Evaluate for Plasmodium parasites.
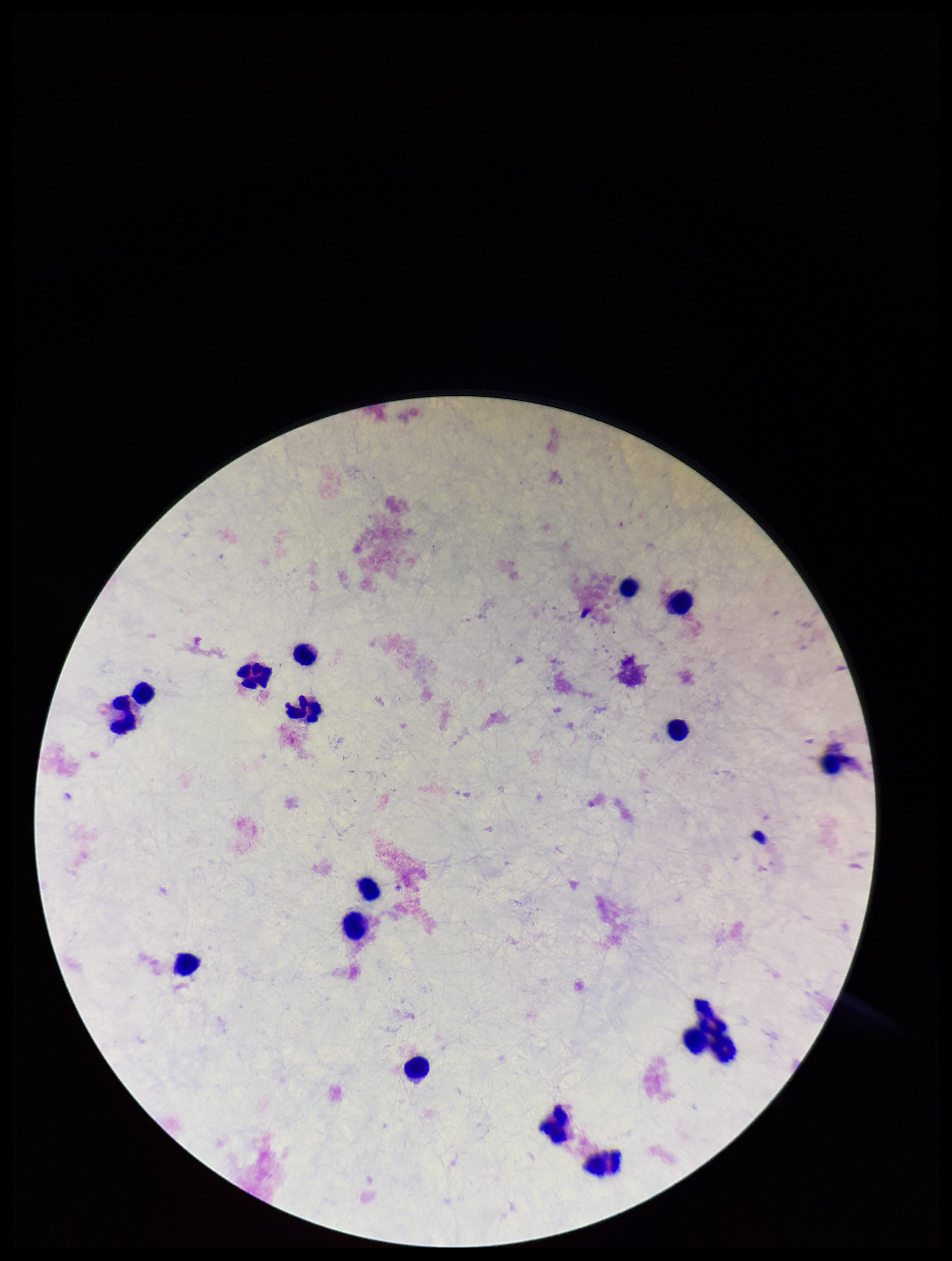
None seen.

Smartphone photograph taken through the eyepiece of a microscope. One field from this slide. Giemsa stain. Leukocyte count: 17. Parasite count: 0. Preparation: thick smear. Patient malaria status: negative. Image is 952×1261 pixels.